Locate every blood parasite and identify its species.
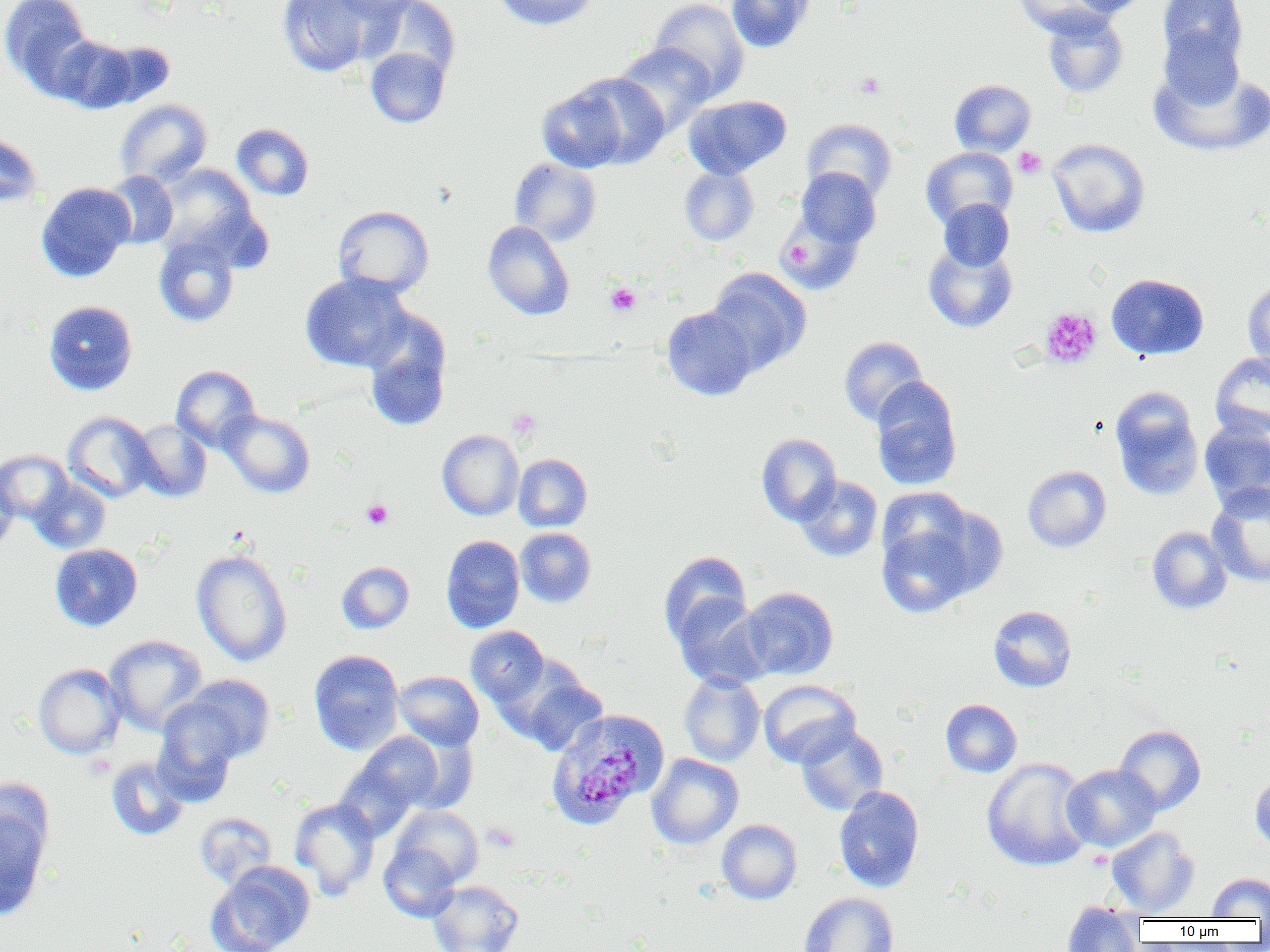
Approximate bounding boxes as (x1, y1, x2, y2) in pixels.
Plasmodium malariae-infected red blood cells: (545, 708, 668, 829).
No Plasmodium falciparum, Plasmodium ovale, Plasmodium vivax, Babesia divergens, or Trypanosoma brucei observed.

slide-level diagnosis = Plasmodium malariae
modality = light microscopy
image size = 1270×952 pixels
preparation = thin blood smear
platelet locations = approximate bounding boxes as (x1, y1, x2, y2) in pixels: (855, 72, 884, 98), (1014, 147, 1046, 178), (782, 240, 815, 267), (605, 282, 641, 316), (1040, 307, 1102, 369), (508, 409, 540, 438), (362, 499, 392, 529), (483, 823, 520, 852)
uninfected red blood cell locations = approximate bounding boxes as (x1, y1, x2, y2) in pixels: (0, 0, 95, 97), (278, 0, 378, 76), (329, 0, 424, 21), (365, 0, 460, 81), (493, 0, 600, 30), (648, 0, 750, 99), (726, 0, 814, 53), (1013, 0, 1115, 38), (1068, 0, 1150, 18), (1158, 0, 1248, 68), (1042, 9, 1128, 98), (1158, 27, 1246, 110), (51, 36, 140, 113), (97, 42, 174, 108), (614, 43, 716, 136), (365, 47, 450, 128), (1149, 65, 1270, 157), (570, 72, 669, 169), (950, 79, 1036, 156), (536, 83, 630, 173), (684, 95, 791, 180), (115, 99, 212, 188), (801, 118, 897, 203), (232, 123, 314, 200), (0, 133, 43, 207), (1047, 138, 1149, 238), (920, 147, 1018, 230), (509, 158, 602, 246), (154, 165, 258, 258), (679, 166, 759, 246), (794, 167, 881, 250), (102, 171, 178, 249), (36, 182, 135, 282), (938, 198, 1015, 271), (333, 205, 433, 298), (778, 207, 866, 296), (483, 221, 574, 320), (154, 236, 239, 326), (923, 241, 1018, 333), (707, 268, 811, 374), (300, 272, 413, 372), (1106, 273, 1208, 360), (1243, 280, 1270, 370), (43, 300, 137, 395), (661, 306, 758, 400), (362, 312, 452, 432), (839, 336, 928, 426), (1210, 352, 1270, 440), (172, 365, 260, 452), (871, 379, 962, 490), (1110, 388, 1204, 501), (220, 409, 315, 498), (63, 411, 156, 503), (1199, 419, 1270, 511), (131, 420, 212, 501), (437, 430, 524, 520), (756, 433, 841, 525), (0, 450, 72, 523), (514, 453, 592, 531), (1022, 465, 1111, 552), (0, 470, 18, 556), (794, 475, 883, 562), (30, 477, 110, 553), (1207, 484, 1270, 587), (876, 516, 980, 618), (1147, 526, 1231, 613), (515, 527, 596, 608), (441, 535, 525, 633), (50, 543, 142, 631), (191, 548, 292, 666), (658, 550, 752, 647), (336, 561, 414, 634), (741, 587, 838, 679), (672, 596, 774, 690), (988, 605, 1076, 692), (465, 625, 550, 708), (104, 635, 207, 735), (309, 649, 404, 754), (33, 663, 125, 759), (394, 670, 484, 750), (515, 671, 609, 757), (678, 671, 765, 767), (184, 674, 274, 763), (759, 680, 860, 768), (940, 699, 1022, 777), (152, 702, 240, 805), (1114, 724, 1206, 816), (796, 725, 888, 816), (398, 730, 480, 814), (354, 731, 445, 814), (647, 753, 744, 848), (106, 756, 189, 840), (981, 757, 1094, 872), (333, 760, 421, 843), (1061, 764, 1161, 852), (1250, 772, 1270, 853), (834, 786, 924, 893), (0, 797, 51, 921), (289, 798, 381, 899), (391, 805, 483, 887), (194, 812, 277, 889), (716, 819, 802, 904), (1106, 827, 1199, 917), (379, 843, 461, 922), (207, 861, 316, 952), (1208, 873, 1270, 919), (428, 880, 523, 952), (799, 892, 898, 952), (1061, 902, 1144, 951)
field of view = one of a larger specimen
magnification = 1000x